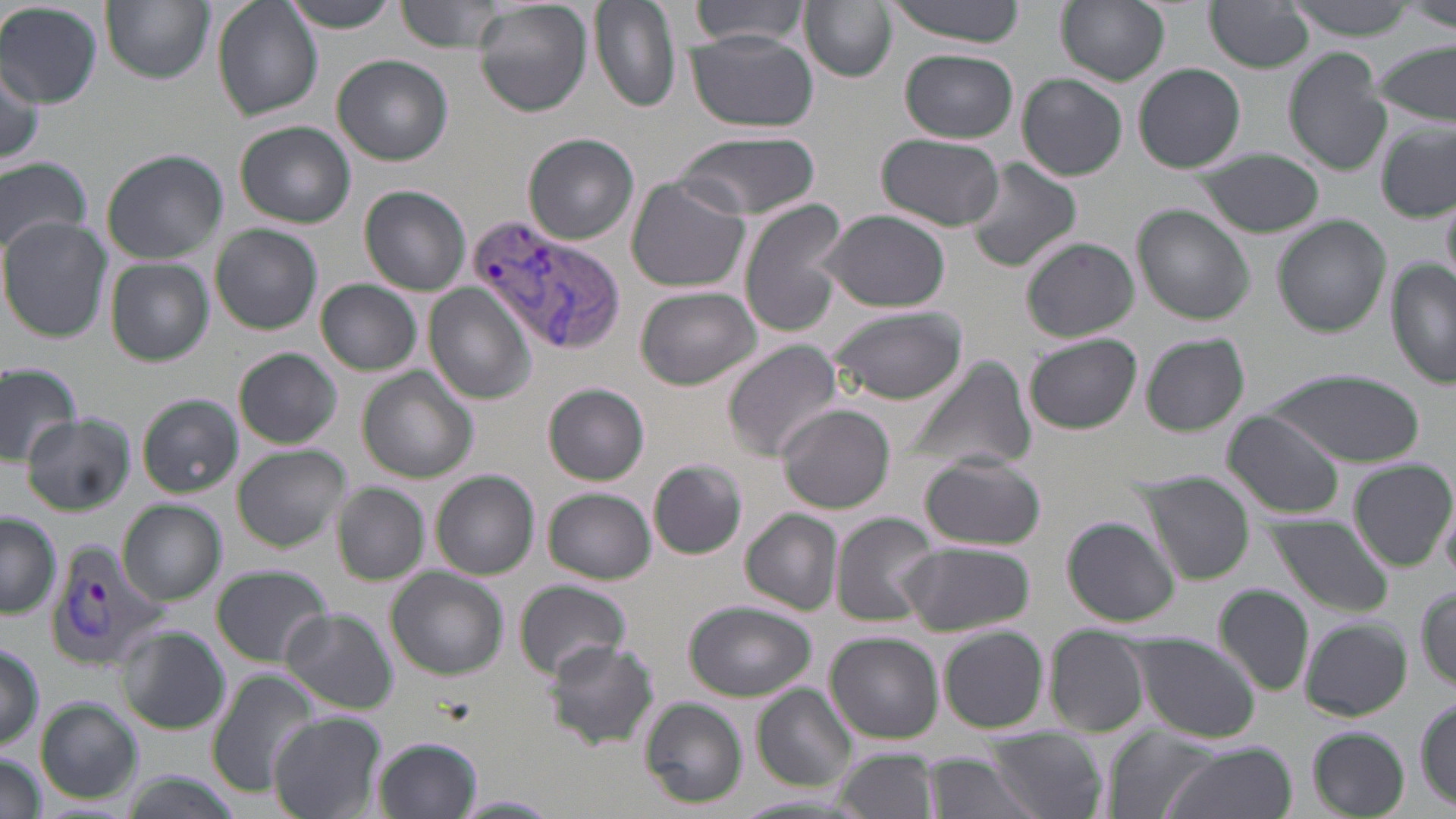

Summary:
  - Coordinate format: approximate bounding boxes as named x1/y1/x2/y2 corners in pixels
  - Uninfected red blood cell locations: (x1=101, y1=0, x2=214, y2=84), (x1=284, y1=0, x2=403, y2=31), (x1=396, y1=0, x2=505, y2=53), (x1=474, y1=0, x2=593, y2=116), (x1=590, y1=0, x2=679, y2=115), (x1=691, y1=0, x2=811, y2=49), (x1=882, y1=0, x2=1032, y2=44), (x1=1056, y1=0, x2=1169, y2=85), (x1=1286, y1=0, x2=1421, y2=38), (x1=212, y1=1, x2=321, y2=120), (x1=802, y1=1, x2=896, y2=83), (x1=1206, y1=1, x2=1315, y2=72), (x1=1404, y1=2, x2=1456, y2=32), (x1=0, y1=3, x2=102, y2=107), (x1=686, y1=33, x2=816, y2=132), (x1=1372, y1=40, x2=1456, y2=126), (x1=901, y1=49, x2=1018, y2=142), (x1=1283, y1=49, x2=1391, y2=176), (x1=333, y1=55, x2=452, y2=165), (x1=0, y1=61, x2=46, y2=167), (x1=1133, y1=64, x2=1246, y2=174), (x1=1018, y1=72, x2=1127, y2=181), (x1=237, y1=122, x2=356, y2=228), (x1=1377, y1=122, x2=1455, y2=222), (x1=678, y1=131, x2=819, y2=220), (x1=523, y1=133, x2=639, y2=245), (x1=878, y1=134, x2=1004, y2=232), (x1=102, y1=149, x2=227, y2=263), (x1=1192, y1=149, x2=1326, y2=238), (x1=0, y1=155, x2=93, y2=256), (x1=962, y1=157, x2=1082, y2=273), (x1=625, y1=175, x2=751, y2=294), (x1=360, y1=185, x2=470, y2=295), (x1=738, y1=198, x2=852, y2=336), (x1=1132, y1=205, x2=1254, y2=326), (x1=816, y1=210, x2=952, y2=313), (x1=1274, y1=217, x2=1391, y2=336), (x1=0, y1=218, x2=111, y2=341), (x1=211, y1=225, x2=323, y2=334), (x1=1022, y1=237, x2=1138, y2=342), (x1=106, y1=258, x2=212, y2=365), (x1=1386, y1=261, x2=1455, y2=390), (x1=315, y1=279, x2=423, y2=376), (x1=425, y1=286, x2=535, y2=402), (x1=635, y1=287, x2=761, y2=390), (x1=829, y1=307, x2=969, y2=405), (x1=1141, y1=333, x2=1250, y2=436), (x1=1025, y1=334, x2=1142, y2=434), (x1=724, y1=340, x2=844, y2=459), (x1=234, y1=348, x2=342, y2=449), (x1=903, y1=355, x2=1036, y2=476), (x1=0, y1=360, x2=80, y2=460), (x1=358, y1=367, x2=477, y2=483), (x1=1264, y1=369, x2=1421, y2=464), (x1=544, y1=383, x2=651, y2=486), (x1=137, y1=394, x2=241, y2=497), (x1=775, y1=403, x2=896, y2=514), (x1=1223, y1=410, x2=1347, y2=518), (x1=21, y1=413, x2=134, y2=514), (x1=231, y1=444, x2=349, y2=550), (x1=919, y1=454, x2=1046, y2=551), (x1=648, y1=459, x2=748, y2=559), (x1=1351, y1=461, x2=1455, y2=571), (x1=431, y1=471, x2=539, y2=580), (x1=1143, y1=480, x2=1255, y2=584), (x1=333, y1=482, x2=428, y2=584), (x1=544, y1=489, x2=655, y2=584), (x1=118, y1=500, x2=227, y2=606), (x1=741, y1=510, x2=843, y2=614), (x1=831, y1=510, x2=939, y2=627), (x1=0, y1=513, x2=61, y2=618), (x1=1264, y1=515, x2=1394, y2=616), (x1=1061, y1=516, x2=1179, y2=626), (x1=898, y1=541, x2=1036, y2=637), (x1=212, y1=563, x2=332, y2=666), (x1=387, y1=567, x2=510, y2=679), (x1=513, y1=580, x2=635, y2=679), (x1=1214, y1=584, x2=1314, y2=698), (x1=1416, y1=586, x2=1455, y2=690), (x1=685, y1=600, x2=815, y2=702), (x1=281, y1=607, x2=397, y2=713), (x1=1301, y1=618, x2=1411, y2=721), (x1=116, y1=627, x2=227, y2=733), (x1=938, y1=628, x2=1051, y2=735), (x1=827, y1=631, x2=944, y2=742), (x1=1043, y1=632, x2=1150, y2=737), (x1=1128, y1=636, x2=1262, y2=744), (x1=541, y1=639, x2=660, y2=751), (x1=0, y1=641, x2=45, y2=751), (x1=208, y1=669, x2=321, y2=795), (x1=754, y1=684, x2=857, y2=790), (x1=637, y1=697, x2=750, y2=809), (x1=1414, y1=697, x2=1455, y2=810), (x1=36, y1=698, x2=142, y2=803), (x1=269, y1=711, x2=387, y2=819), (x1=1307, y1=726, x2=1409, y2=818), (x1=985, y1=727, x2=1105, y2=818), (x1=1107, y1=729, x2=1217, y2=819), (x1=373, y1=736, x2=483, y2=819), (x1=1156, y1=740, x2=1295, y2=819), (x1=837, y1=746, x2=941, y2=819), (x1=921, y1=751, x2=1039, y2=819), (x1=0, y1=754, x2=49, y2=819), (x1=453, y1=793, x2=559, y2=817)
  - Plasmodium vivax-infected red blood cell locations: (x1=469, y1=215, x2=629, y2=358), (x1=44, y1=542, x2=169, y2=670)
  - Slide-level diagnosis: Plasmodium vivax
  - Modality: optical microscopy
  - Preparation: thin blood film
  - Image size: 1456×819 pixels
  - Field of view: single
  - Magnification: 1000x
  - Stain: May-Grünwald-Giemsa